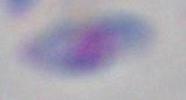 Captured at 1000x magnification. Photomicrograph. Toxoplasma gondii is shown.